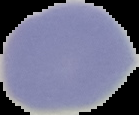

{
  "result": "no malaria parasites detected",
  "image_type": "cell region segmented out of the field of view; surrounding area masked to black",
  "image_size": "139×115 pixels",
  "preparation": "thin blood smear"
}